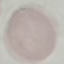 Malaria status: uninfected. Thin smear of blood. Cell patch, automatically extracted from a larger field of view and resized to 64 × 64 pixels. Giemsa stain. Photographed with a smartphone camera at the microscope eyepiece.